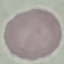
malaria_status: uninfected
preparation: thin blood film
stain: Giemsa
capture: smartphone camera at the microscope eyepiece
image_type: cell patch, automatically extracted from a larger field of view and resized to 64 × 64 pixels